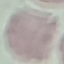 Result: negative for malaria parasites. Thin blood film. Cell patch, automatically extracted from a larger field of view and resized to 64 × 64 pixels. Acquired by smartphone through the microscope eyepiece. Giemsa stain.